Report the malaria status of this cell.
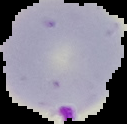
Parasitized.

image type = cell region segmented out of the field of view; surrounding area masked to black
preparation = thin blood film
image size = 127×124 pixels